Find the cells and give the type of each one.
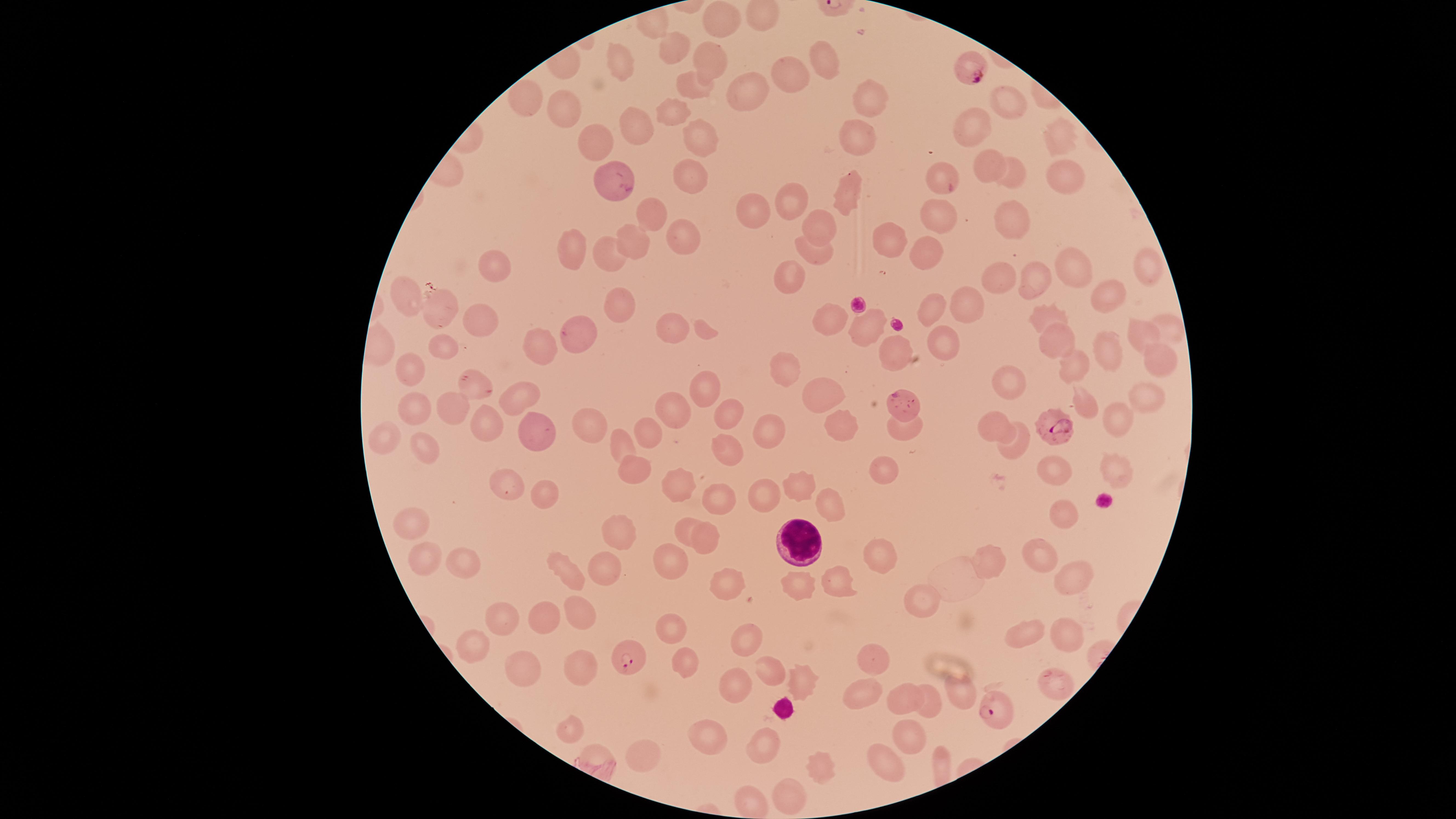
Approximate marker points as (x, y) in pixels.
Parasitized red blood cells: (975, 72), (614, 180), (900, 402), (1052, 423), (630, 660), (991, 709).
Uninfected red blood cells: (722, 22), (672, 44), (616, 62), (710, 62), (824, 63), (789, 77), (695, 86), (746, 96), (871, 97), (524, 100), (1006, 102), (566, 109), (673, 114), (637, 125), (973, 127), (702, 139), (858, 141), (1056, 141), (596, 142), (988, 165), (1019, 174), (1062, 174), (689, 178), (941, 182), (849, 196), (792, 206), (654, 212), (938, 212), (1007, 212), (752, 214), (821, 226), (680, 233), (635, 244), (891, 244), (569, 245), (609, 253), (926, 253), (814, 255), (1147, 264), (491, 265), (1070, 271), (789, 280), (999, 281), (1032, 281), (410, 297), (1109, 300), (965, 304), (619, 306), (930, 309), (1043, 311), (436, 313), (481, 319), (833, 322), (669, 328), (1169, 328), (868, 329), (580, 333), (1057, 335), (1141, 338), (439, 343), (542, 343), (945, 345), (1108, 351), (894, 354), (1157, 361), (413, 364), (1076, 366), (784, 369), (1012, 381), (470, 387), (702, 389), (818, 391), (518, 392), (1146, 397), (1084, 402), (445, 404), (414, 405), (672, 406), (728, 411), (1113, 417), (840, 421), (483, 422), (589, 424), (990, 424), (907, 426), (771, 429), (542, 430), (649, 436), (384, 439), (622, 441), (1015, 446), (427, 447), (725, 447), (1113, 467), (1055, 468), (883, 469), (631, 473), (509, 482), (799, 488), (676, 489), (544, 493), (716, 496), (765, 500), (839, 505), (1062, 514), (417, 527), (685, 528), (617, 529), (705, 535), (1043, 552), (876, 555), (425, 560), (673, 560), (991, 561), (463, 565), (569, 569), (605, 570), (1069, 574), (840, 584), (729, 586), (800, 588), (580, 604), (917, 604), (504, 617), (553, 621), (668, 626), (1029, 630), (747, 636), (1065, 639), (470, 643), (870, 663), (524, 665), (682, 665), (580, 667), (769, 668), (800, 681), (733, 688), (905, 690), (957, 691), (859, 698), (928, 705), (568, 732), (909, 737), (764, 739), (705, 740), (640, 755), (817, 764), (891, 764), (789, 795), (748, 801).
White blood cells: (797, 538).

visible region = circular
image size = 1456×819 pixels
preparation = thin smear of blood
species = Plasmodium falciparum
stain = Giemsa
capture = smartphone photograph through the microscope eyepiece
field of view = single